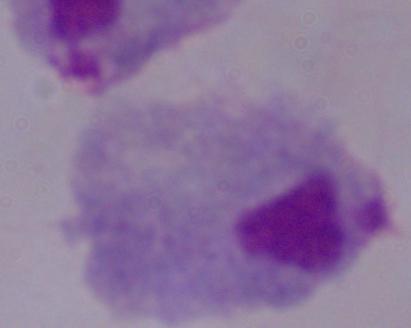

Micrograph. 1000x magnification. A trichomonad is shown.